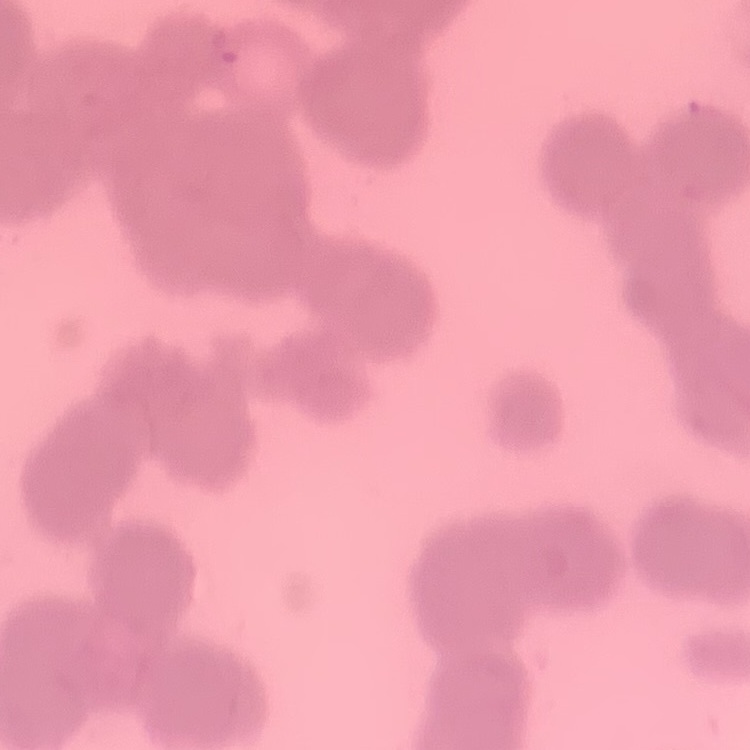
{
  "erythrocyte_morphology": "rouleaux formation",
  "stain": "Field's or Giemsa",
  "preparation": "thin blood smear",
  "image_type": "square crop of a larger photomicrograph"
}